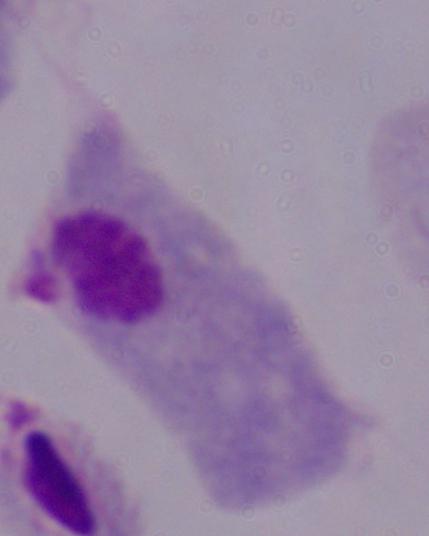
1000x magnification. Photomicrograph. A trichomonad is seen.